Point out each Plasmodium parasite.
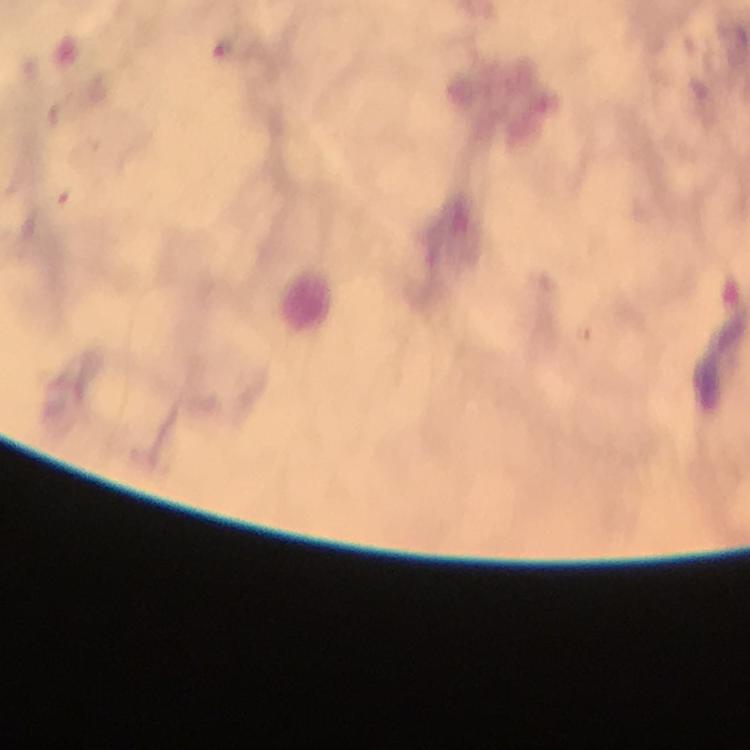

Approximate centers as (x, y) in pixels.
Plasmodium parasites: (224, 48).

{
  "immersion_oil": "applied",
  "preparation": "thick blood smear",
  "capture": "smartphone mounted on the microscope",
  "cropped_from": "a single field of view",
  "magnification": "100x",
  "stain": "Giemsa",
  "image_size": "750×750 pixels",
  "context": "from a malaria diagnostic workup"
}